Describe the morphology of the erythrocytes.
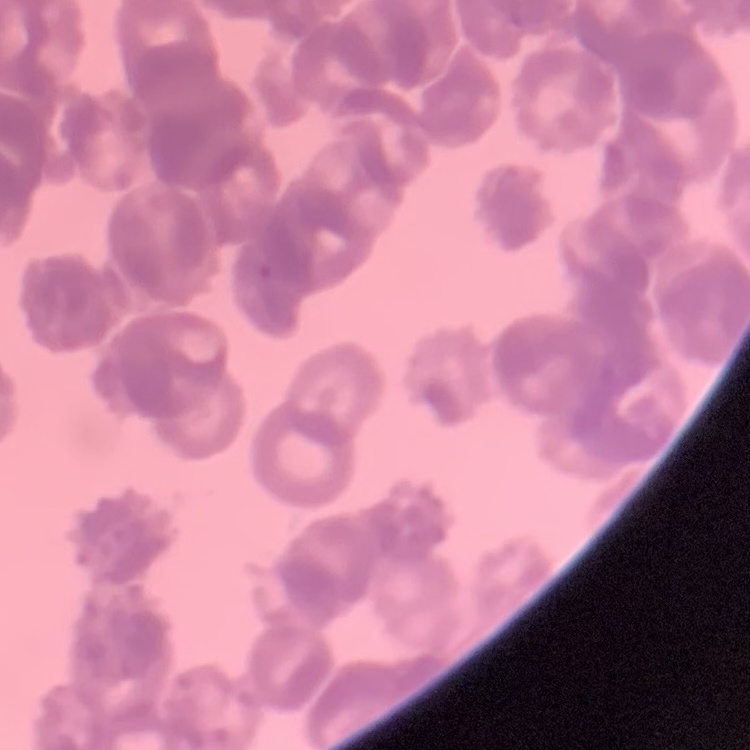
Rouleaux formation.

Field's or Giemsa stain. Square crop of a larger photomicrograph. Thin blood smear.